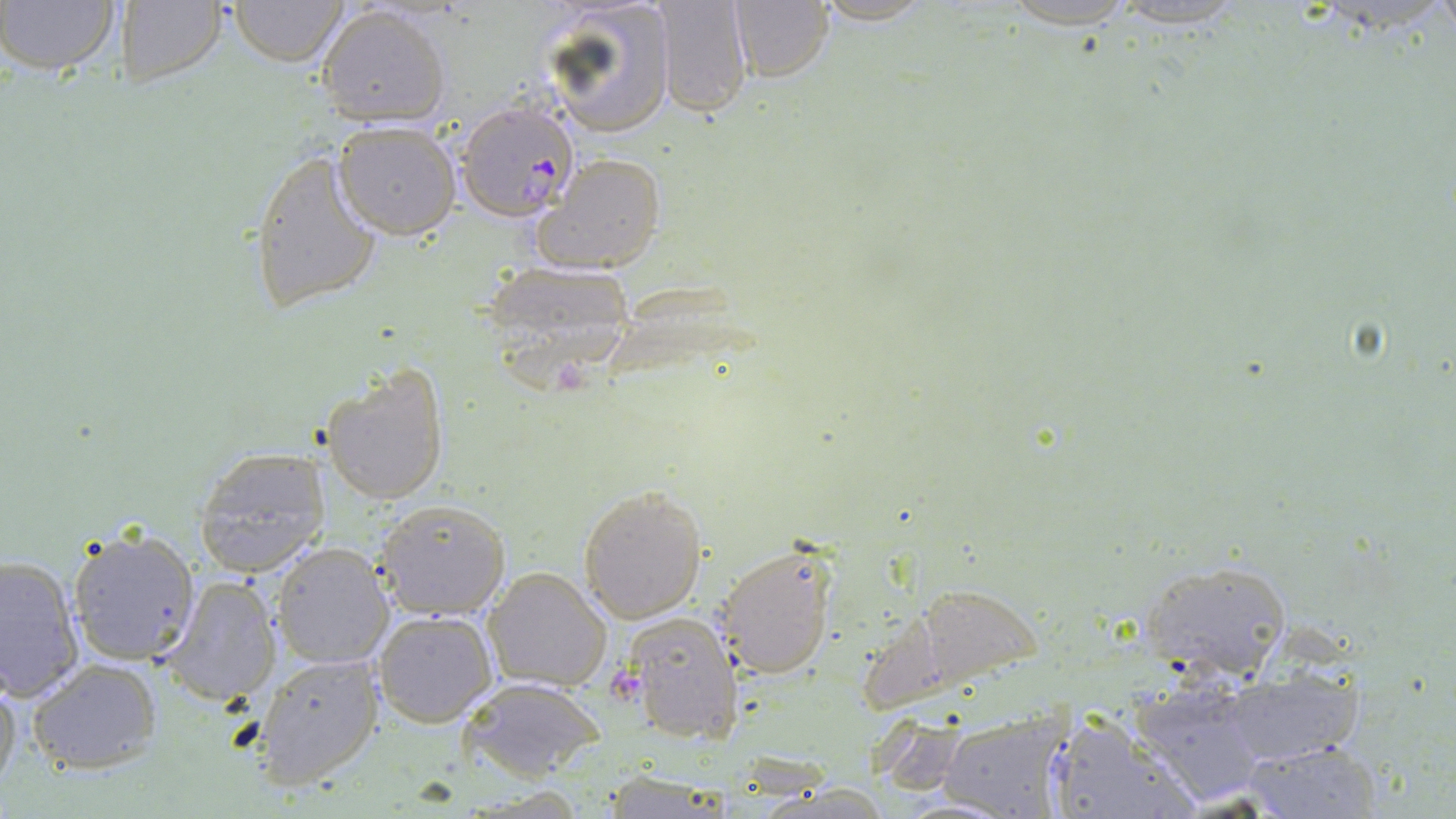

Approximate bounding boxes as [x1, y1, x2, y2] in pixels. Plasmodium falciparum-infected red blood cell locations: [454, 102, 583, 224]. Uninfected red blood cell locations: [2, 0, 124, 77], [226, 0, 349, 66], [538, 0, 677, 136], [807, 0, 938, 26], [1106, 0, 1256, 31], [108, 1, 228, 88], [651, 1, 752, 119], [727, 1, 835, 83], [316, 6, 450, 127], [330, 120, 461, 240], [246, 145, 386, 314], [534, 153, 667, 276], [478, 257, 641, 384], [321, 363, 450, 506], [193, 446, 334, 578], [578, 485, 707, 623], [376, 498, 511, 619], [67, 528, 200, 667], [711, 540, 839, 680], [271, 544, 394, 670], [0, 552, 86, 702], [1138, 560, 1291, 677], [482, 567, 612, 692], [159, 573, 285, 707], [371, 608, 498, 728], [621, 612, 743, 746], [252, 652, 384, 787], [28, 658, 162, 776], [1219, 669, 1366, 768], [0, 671, 21, 798], [458, 675, 605, 780], [1126, 679, 1272, 805], [939, 710, 1063, 819], [1059, 710, 1200, 819], [1238, 740, 1384, 819]. Platelet locations: [611, 671, 641, 705]. Slide-level diagnosis: Plasmodium falciparum. Optical microscopy. Captured at 1000x magnification. May-Grünwald-Giemsa-stained preparation. Thin blood film. One field of a larger specimen. Image is 1456×819 pixels.